Point out each leukocyte.
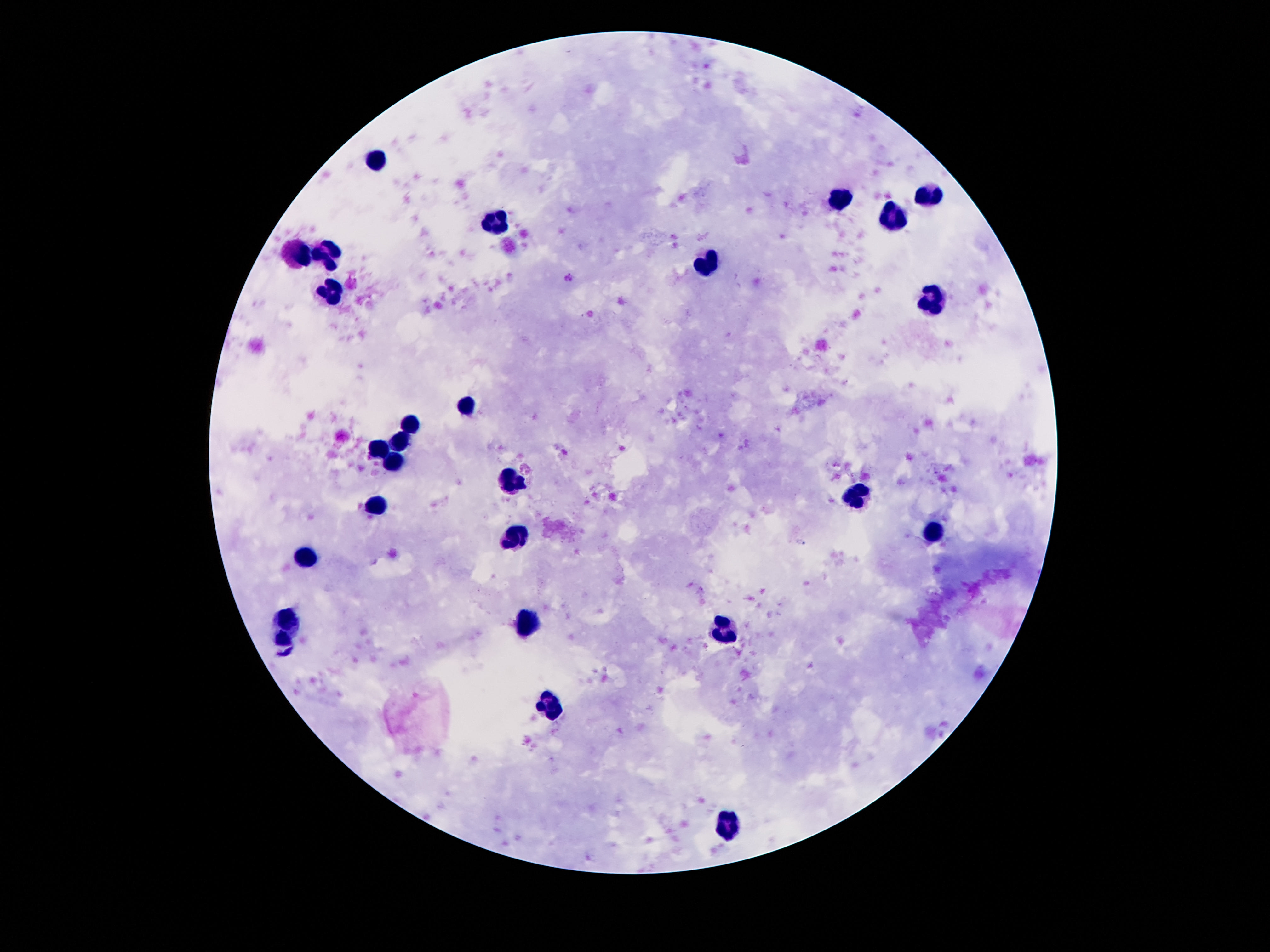

Approximate centers as {x, y} in pixels.
Leukocytes: {375, 160}, {932, 195}, {838, 201}, {892, 216}, {494, 222}, {296, 253}, {328, 255}, {706, 265}, {332, 292}, {932, 300}, {466, 404}, {409, 425}, {400, 444}, {379, 451}, {395, 465}, {514, 482}, {855, 492}, {379, 506}, {932, 533}, {515, 540}, {303, 557}, {288, 617}, {528, 626}, {725, 628}, {279, 641}, {552, 707}, {729, 824}.

Thick peripheral-blood smear. Photographed through the microscope eyepiece with a smartphone camera. Patient malaria status: not infected. 100x magnification. Giemsa stain. One field from this slide. Image is 1270×952 pixels.